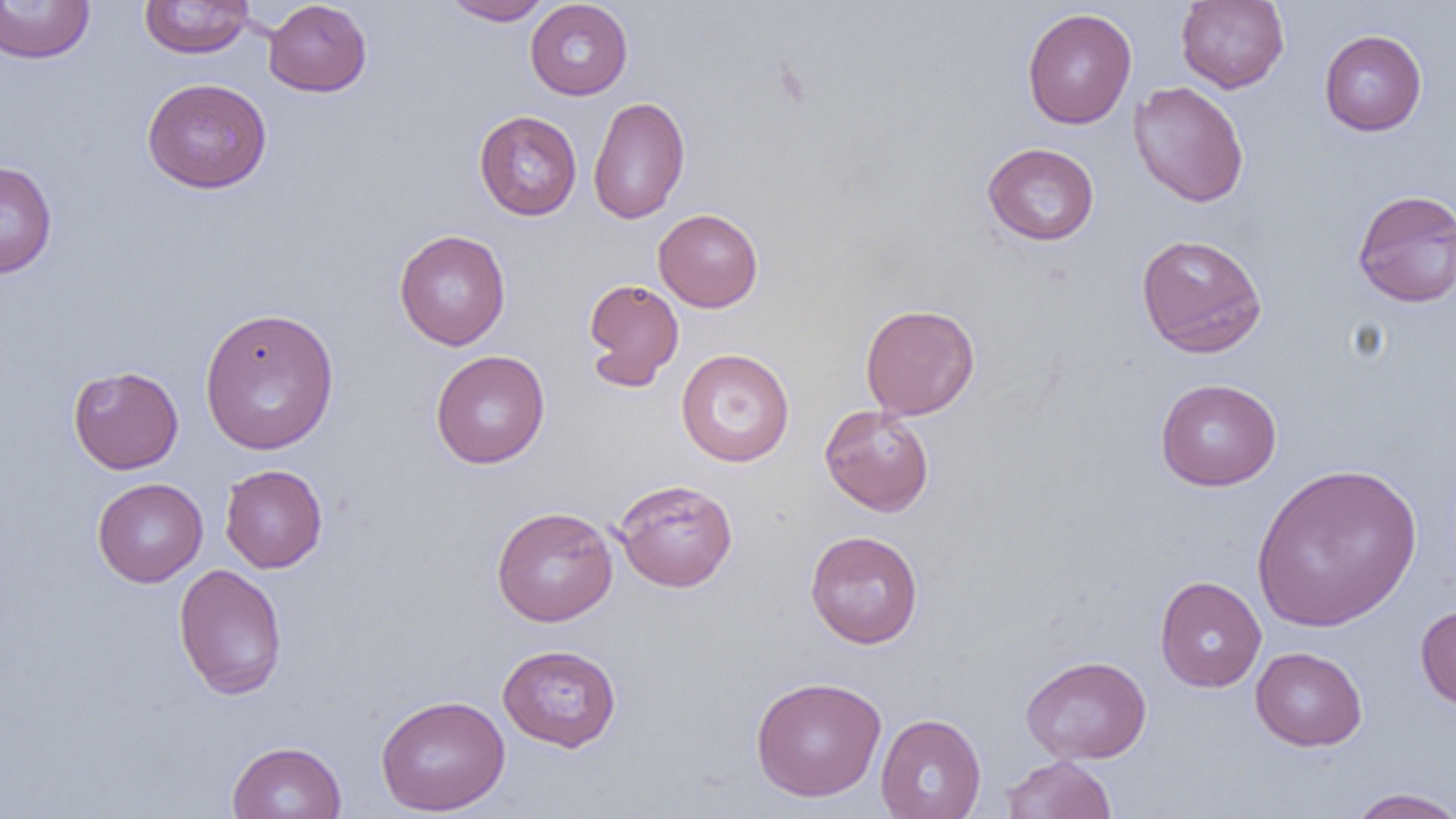
Approximate bounding boxes as (x1, y1, x2, y2) in pixels. Uninfected red blood cell locations: (441, 0, 554, 25), (1176, 0, 1289, 93), (0, 1, 95, 64), (139, 1, 254, 58), (263, 1, 372, 97), (525, 1, 633, 100), (1022, 7, 1137, 130), (1319, 29, 1427, 136), (141, 77, 273, 194), (1129, 81, 1249, 208), (588, 95, 690, 224), (474, 110, 582, 220), (982, 142, 1100, 246), (0, 160, 58, 279), (1352, 188, 1456, 308), (653, 208, 763, 312), (394, 229, 511, 350), (1136, 233, 1267, 358), (583, 278, 684, 391), (860, 303, 980, 420), (199, 307, 340, 455), (676, 349, 795, 468), (430, 350, 550, 469), (67, 365, 184, 474), (1155, 377, 1282, 491), (819, 404, 935, 516), (1250, 462, 1422, 632), (219, 463, 328, 573), (92, 477, 208, 587), (613, 479, 738, 592), (491, 506, 618, 626), (805, 530, 923, 649), (173, 563, 288, 701), (1154, 575, 1266, 692), (1415, 602, 1456, 713), (497, 643, 623, 752), (1250, 647, 1367, 751), (1021, 655, 1152, 764), (749, 676, 887, 801), (375, 694, 510, 816), (875, 713, 986, 819), (226, 741, 347, 819), (1000, 755, 1117, 818), (1345, 787, 1456, 819). Slide-level diagnosis: negative for blood parasites. 1000x magnification. Thin blood film. Single field of view. Image is 1456×819 pixels. Light microscopy.